Locate every blood parasite and identify its species.
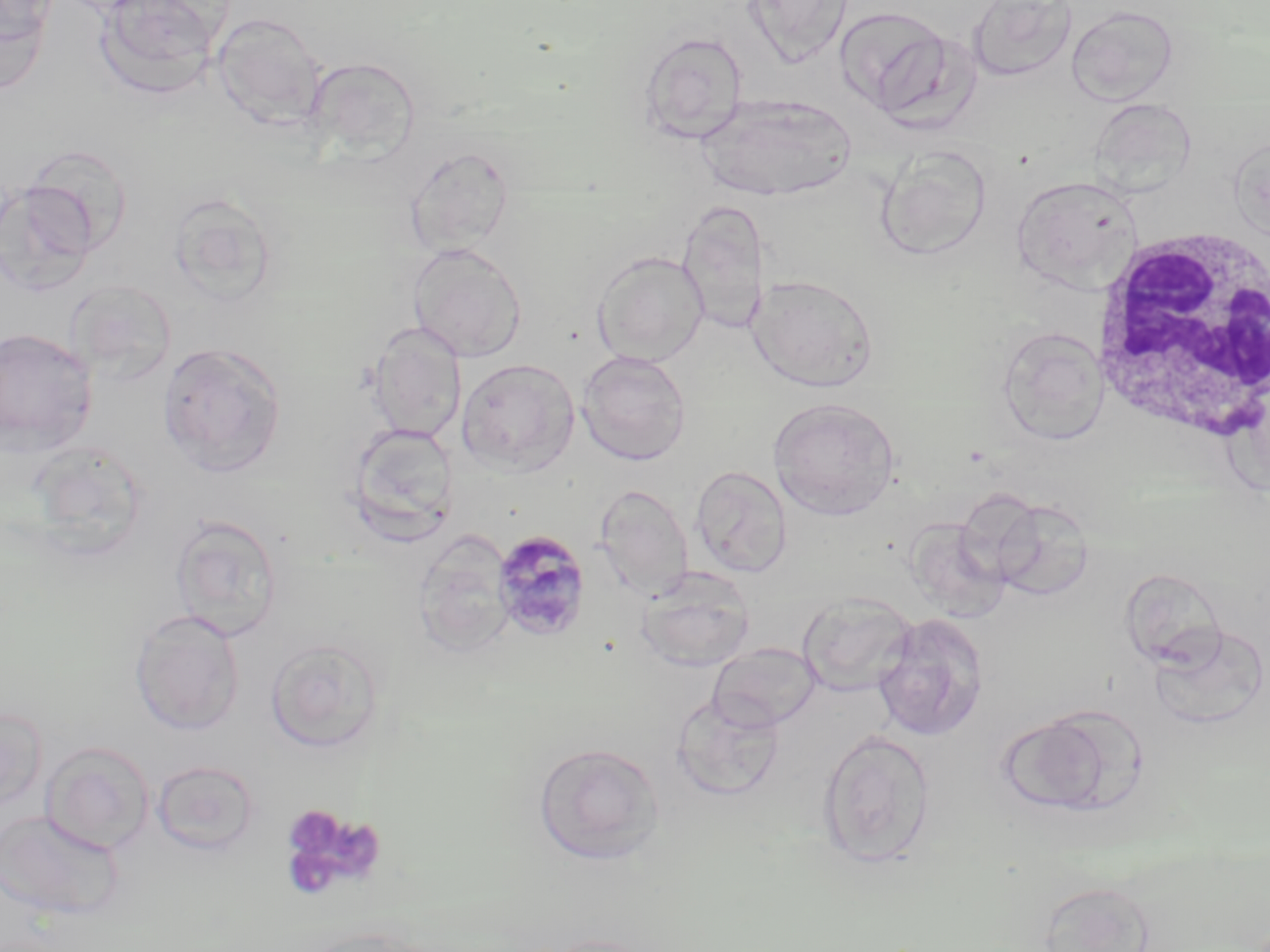
Approximate bounding boxes as (x1,y1)-(x2,y2) corner pairs in pixels.
Plasmodium malariae-infected red blood cells: (491,529)-(593,642).
No Plasmodium falciparum, Plasmodium ovale, Plasmodium vivax, Babesia divergens, or Trypanosoma brucei observed.

slide-level diagnosis = Plasmodium malariae
magnification = 1000x
platelet locations = approximate bounding boxes as (x1,y1)-(x2,y2) corner pairs in pixels: (280,806)-(387,897)
preparation = thin blood film
image size = 1270×952 pixels
uninfected red blood cell locations = approximate bounding boxes as (x1,y1)-(x2,y2) corner pairs in pixels: (0,0)-(59,45), (95,0)-(227,98), (742,0)-(854,66), (967,0)-(1077,82), (0,1)-(54,95), (836,6)-(951,116), (1067,6)-(1179,106), (211,13)-(327,127), (637,31)-(748,144), (303,56)-(422,165), (699,95)-(857,202), (1089,99)-(1197,198), (1227,134)-(1270,241), (16,143)-(133,259), (405,145)-(516,256), (876,145)-(993,260), (1011,174)-(1142,292), (0,181)-(98,298), (168,191)-(280,306), (676,199)-(770,334), (407,242)-(526,362), (592,250)-(709,367), (748,274)-(879,392), (64,279)-(178,386), (368,322)-(466,443), (997,326)-(1109,444), (0,327)-(99,453), (157,342)-(286,478), (577,350)-(692,466), (457,358)-(579,475), (769,398)-(901,520), (346,422)-(460,545), (690,465)-(792,577), (594,484)-(694,599), (984,494)-(1094,601), (168,513)-(283,641), (905,516)-(1010,621), (413,531)-(515,659), (637,567)-(755,672), (797,591)-(917,696), (129,609)-(245,736), (872,613)-(989,742), (1149,624)-(1269,730), (265,638)-(385,752), (709,642)-(822,731), (671,693)-(784,801), (0,706)-(47,814), (998,715)-(1111,816), (816,728)-(935,869), (41,741)-(154,855), (533,742)-(664,865), (151,760)-(260,857), (0,809)-(124,920), (1038,879)-(1157,952), (539,933)-(663,952)
white blood cell locations = approximate bounding boxes as (x1,y1)-(x2,y2) corner pairs in pixels: (1086,217)-(1270,449)
stain = May-Grünwald-Giemsa
field of view = one of a larger specimen
modality = light microscopy